Comment on the morphology of the erythrocytes.
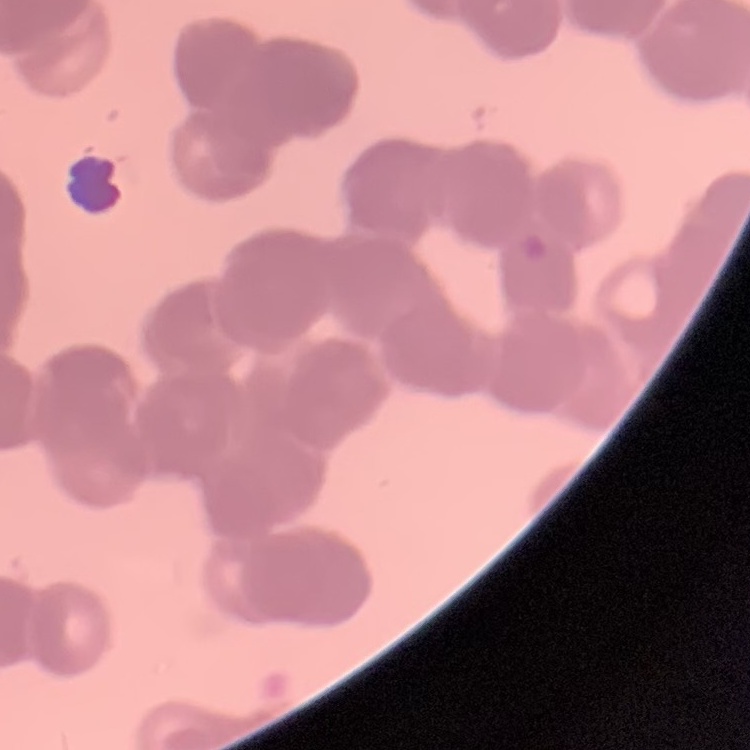

Rouleaux formation.

{
  "image_type": "one tile cut from a larger photomicrograph",
  "stain": "Field's or Giemsa",
  "preparation": "thin blood smear"
}